State which parasite is depicted.
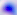
Toxoplasma gondii.

400x magnification. Micrograph.